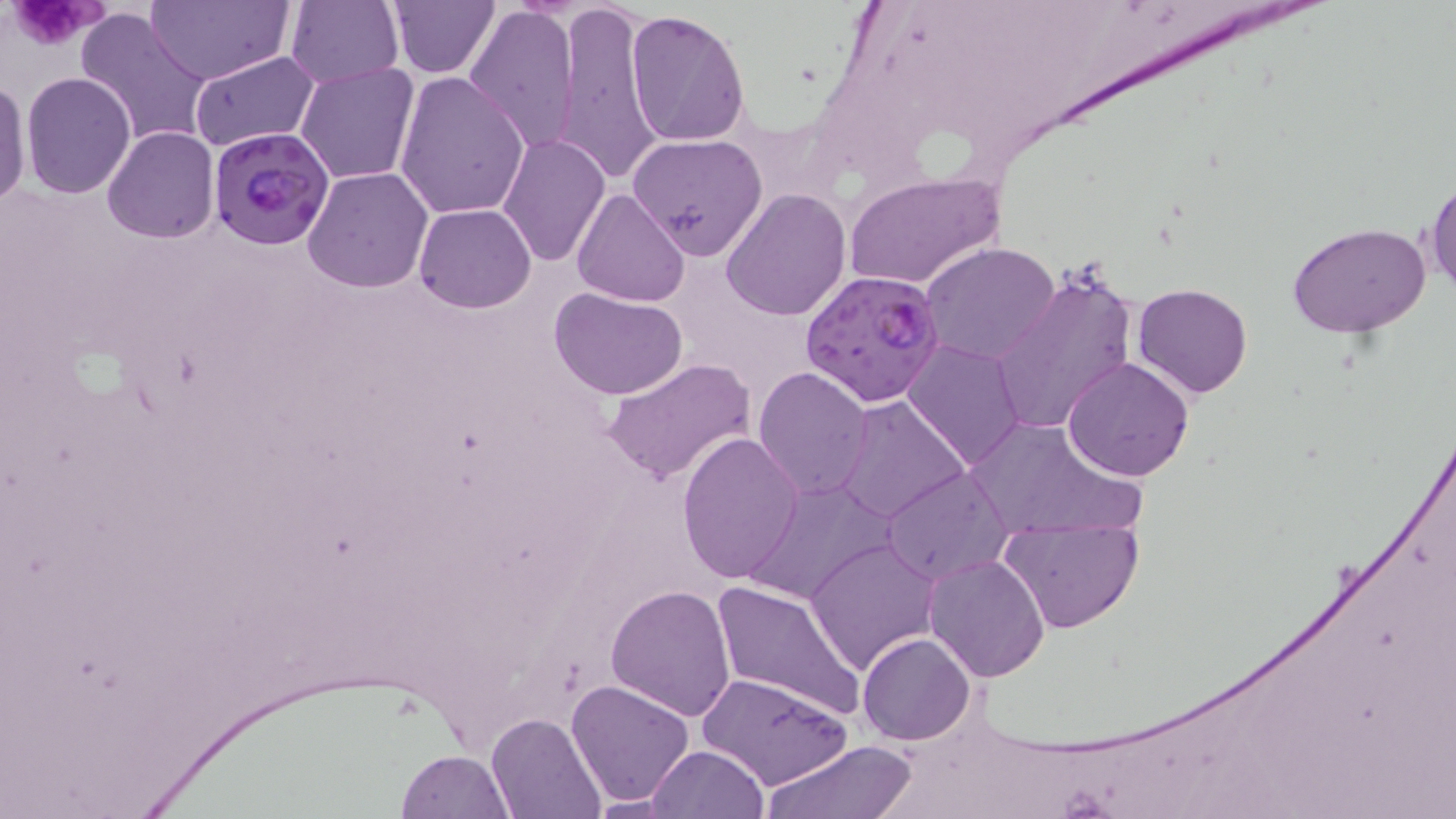

Summary:
  - Coordinate format: approximate bounding boxes as (x1, y1, x2, y2) in pixels
  - Uninfected red blood cell locations: (147, 0, 291, 84), (286, 0, 404, 89), (388, 0, 502, 78), (554, 0, 666, 188), (464, 3, 582, 151), (76, 6, 213, 149), (623, 8, 751, 145), (190, 49, 319, 153), (296, 63, 419, 185), (393, 70, 531, 218), (21, 71, 135, 197), (0, 77, 31, 207), (103, 127, 219, 243), (628, 132, 767, 260), (497, 134, 610, 264), (302, 166, 433, 294), (843, 171, 1004, 290), (1424, 176, 1455, 297), (572, 187, 690, 307), (722, 187, 852, 321), (413, 204, 537, 312), (1286, 222, 1431, 337), (920, 242, 1062, 367), (988, 263, 1141, 438), (1134, 282, 1254, 400), (549, 284, 691, 401), (902, 337, 1026, 470), (1062, 356, 1196, 481), (601, 358, 756, 486), (752, 366, 875, 503), (832, 396, 969, 525), (961, 416, 1135, 542), (676, 431, 804, 586), (881, 465, 1016, 587), (741, 481, 894, 603), (999, 514, 1142, 634), (805, 537, 940, 674), (924, 554, 1052, 682), (709, 578, 866, 721), (606, 584, 736, 719), (858, 632, 975, 744), (697, 671, 852, 790), (567, 677, 693, 806), (488, 712, 605, 819), (762, 738, 920, 819), (646, 745, 767, 819), (394, 751, 513, 819)
  - Platelet locations: (10, 0, 105, 50)
  - Plasmodium falciparum-infected red blood cell locations: (207, 124, 336, 250), (800, 268, 948, 407)
  - Slide-level diagnosis: Plasmodium falciparum
  - Image size: 1456×819 pixels
  - Modality: optical microscopy
  - Preparation: thin blood smear
  - Magnification: 1000x
  - Field of view: one of a larger specimen
  - Stain: May-Grünwald-Giemsa